Name the parasite shown.
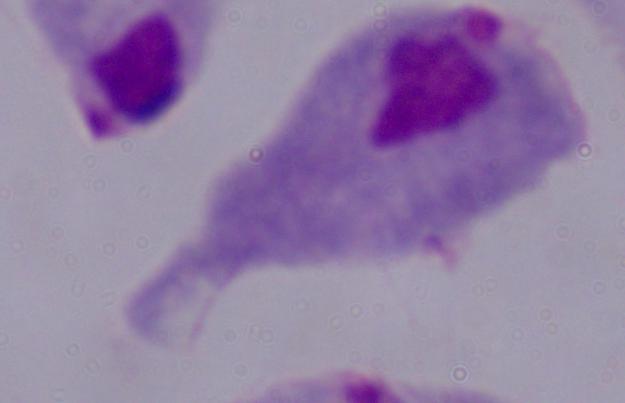
This is a trichomonad.

Summary:
  - Magnification: 1000x
  - Modality: photomicrograph